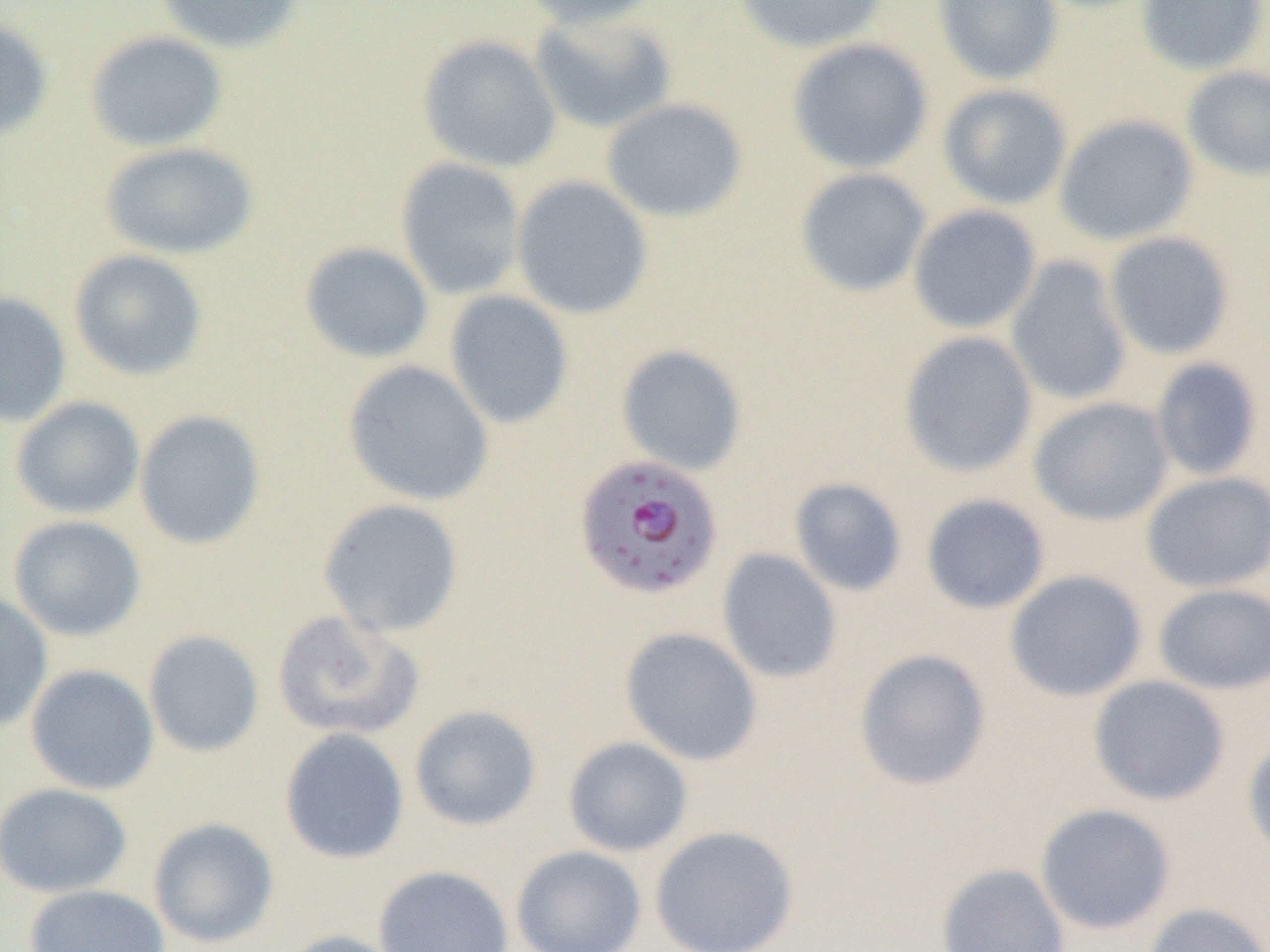
{
  "slide_level_diagnosis": "Plasmodium falciparum",
  "magnification": "1000x",
  "plasmodium_falciparum_infected_red_blood_cell_locations": "approximate bounding boxes as (x1,y1)-(x2,y2) corner pairs in pixels: (573,453)-(724,601)",
  "modality": "light microscopy",
  "preparation": "thin blood film",
  "field_of_view": "one of a larger specimen",
  "uninfected_red_blood_cell_locations": "approximate bounding boxes as (x1,y1)-(x2,y2) corner pairs in pixels: (153,0)-(306,55), (519,0)-(668,30), (733,0)-(889,54), (932,0)-(1064,86), (1136,0)-(1268,75), (530,10)-(677,134), (0,15)-(54,144), (84,30)-(228,152), (417,34)-(562,173), (786,37)-(934,174), (1181,66)-(1270,181), (937,84)-(1072,210), (601,98)-(748,222), (1054,114)-(1198,247), (99,141)-(259,260), (396,157)-(526,300), (794,167)-(931,297), (511,175)-(654,320), (907,204)-(1042,334), (1104,231)-(1235,359), (299,241)-(435,364), (68,249)-(208,381), (1005,256)-(1134,406), (444,290)-(574,430), (0,291)-(72,427), (898,331)-(1038,478), (615,343)-(748,476), (1150,358)-(1263,480), (342,360)-(495,506), (10,396)-(145,519), (1029,396)-(1174,526), (134,409)-(266,550), (1140,471)-(1270,593), (789,477)-(908,597), (920,493)-(1051,614), (317,498)-(465,637), (8,515)-(147,642), (717,548)-(843,684), (1004,569)-(1148,702), (1153,583)-(1270,695), (0,589)-(53,732), (270,610)-(424,742), (619,626)-(763,766), (143,630)-(265,758), (853,648)-(992,791), (25,663)-(159,796), (1088,675)-(1230,806), (409,705)-(542,831), (279,728)-(410,864), (1242,733)-(1270,862), (563,736)-(693,857), (0,782)-(133,898), (1034,803)-(1176,935), (147,817)-(279,949), (649,825)-(800,952), (510,845)-(647,952), (935,862)-(1071,952), (373,864)-(514,952), (23,884)-(170,952), (1142,902)-(1270,952), (276,929)-(409,952)",
  "image_size": "1270×952 pixels"
}